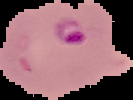

Summary:
  - Image size: 133×100 pixels
  - Preparation: thin blood smear
  - Result: malaria parasites identified
  - Image type: segmented cell region with the area outside set to black